Comment on the morphology of the erythrocytes.
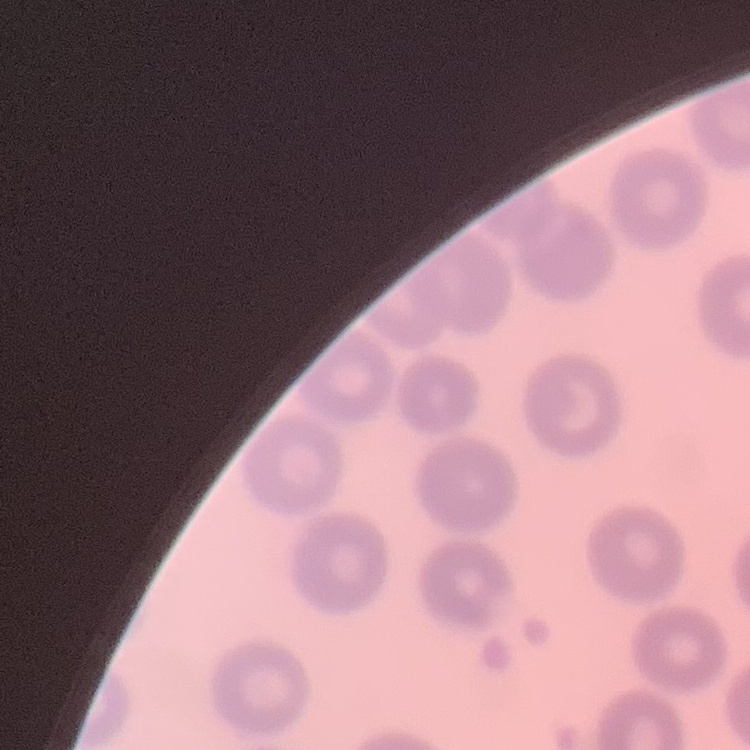
They show no rouleaux formation.

preparation = thin peripheral smear
stain = Field's or Giemsa
image type = square crop of a larger photomicrograph